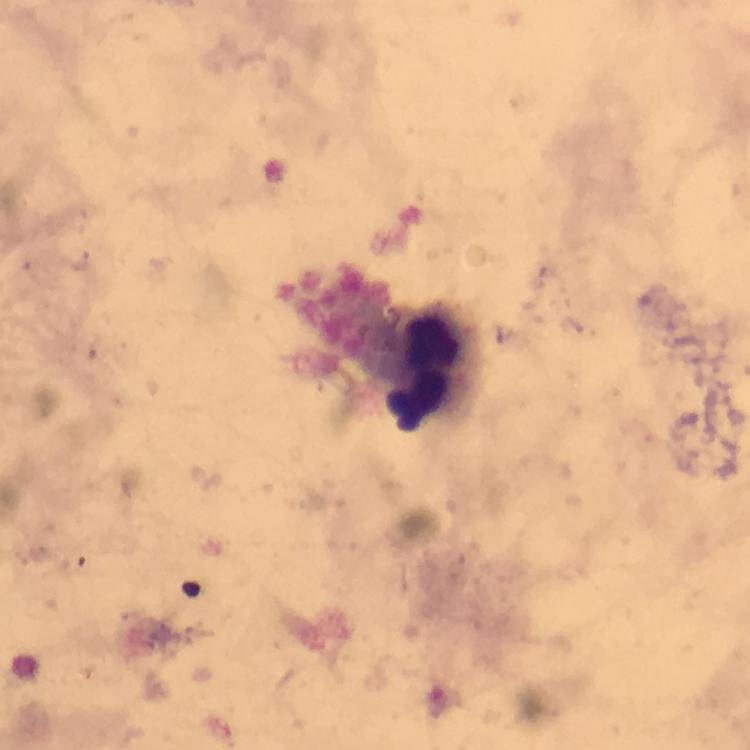
Approximate centers as (x, y) in pixels. Leukocyte locations: (423, 373). Giemsa-stained preparation. Smartphone photograph taken through a microscope. Thick blood smear. Image is 750×750 pixels. From a malaria diagnostic workup. A crop from one field of view. Plasmodium parasites: none detected. At 100x magnification. Immersion oil applied.